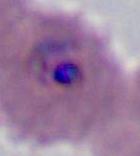

Summary:
  - Identification: Plasmodium
  - Modality: micrograph
  - Magnification: 400x or 1000x